Name the parasite shown.
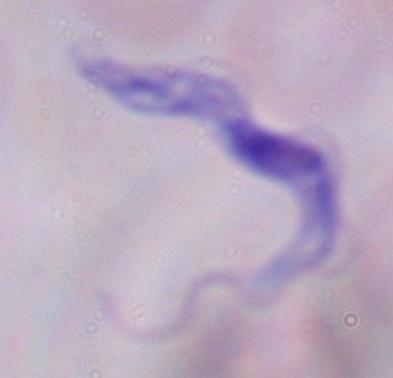
This is a trypanosome.

Summary:
  - Magnification: 1000x
  - Modality: micrograph